Classify this cell by malaria status.
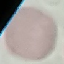

It is uninfected.

Summary:
  - Image type: cell patch, automatically extracted from a larger field of view and resized to 64 × 64 pixels
  - Preparation: thin smear
  - Capture: smartphone camera at the microscope eyepiece
  - Stain: Giemsa